Locate every blood parasite and identify its species.
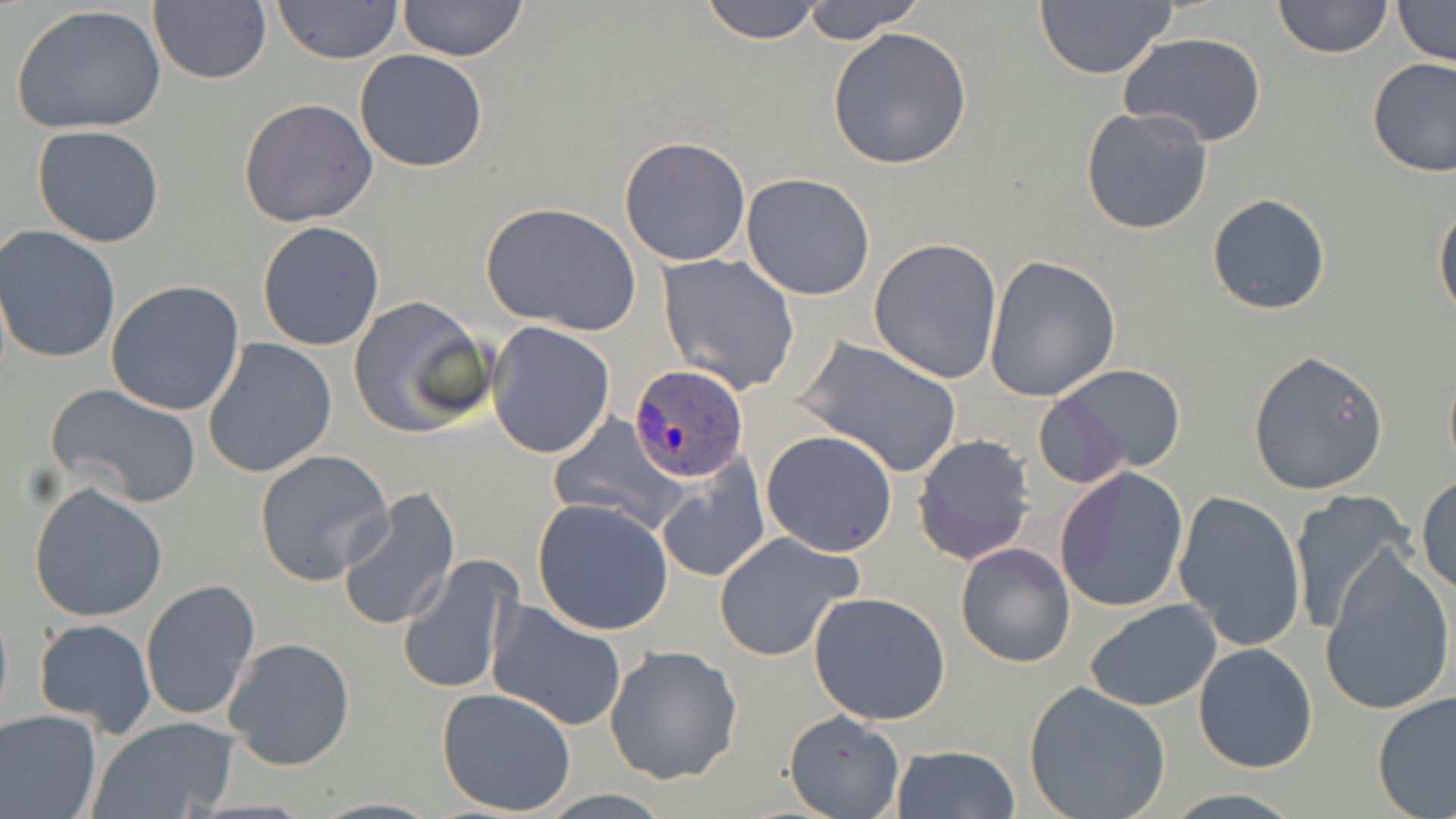

Approximate bounding boxes as [x1, y1, x2, y2] in pixels.
Plasmodium ovale-infected red blood cells: [628, 363, 749, 482].
No Plasmodium falciparum, Plasmodium malariae, Plasmodium vivax, Babesia divergens, or Trypanosoma brucei observed.

Uninfected red blood cell locations: [149, 0, 272, 85], [396, 0, 530, 63], [699, 0, 828, 43], [798, 0, 927, 43], [1273, 0, 1393, 58], [1391, 0, 1456, 67], [271, 1, 404, 65], [1034, 2, 1177, 79], [8, 3, 167, 137], [826, 27, 972, 168], [1119, 33, 1267, 148], [355, 48, 489, 172], [1365, 57, 1456, 177], [238, 98, 378, 228], [1081, 107, 1214, 235], [31, 124, 166, 247], [618, 135, 752, 267], [741, 173, 876, 301], [1206, 193, 1331, 315], [1433, 199, 1456, 326], [481, 201, 641, 336], [257, 221, 385, 351], [0, 226, 122, 365], [869, 237, 1002, 384], [657, 253, 800, 394], [983, 255, 1120, 402], [105, 280, 246, 416], [347, 296, 492, 439], [486, 323, 616, 458], [798, 335, 963, 478], [202, 338, 337, 478], [1246, 349, 1389, 496], [1442, 360, 1456, 482], [1042, 364, 1188, 479], [46, 382, 202, 509], [548, 414, 686, 534], [761, 430, 898, 557], [911, 433, 1035, 566], [253, 448, 394, 586], [655, 457, 771, 581], [1053, 465, 1190, 614], [1416, 475, 1455, 593], [28, 481, 169, 623], [334, 489, 460, 633], [1173, 489, 1307, 651], [1287, 492, 1416, 636], [532, 499, 674, 636], [712, 530, 865, 663], [954, 541, 1075, 669], [1320, 546, 1455, 718], [398, 555, 521, 696], [139, 580, 261, 725], [807, 590, 953, 726], [484, 600, 628, 731], [1084, 600, 1222, 712], [32, 618, 157, 738], [222, 636, 355, 771], [1193, 641, 1319, 774], [604, 644, 742, 785], [1023, 681, 1172, 819], [436, 687, 577, 817], [1372, 691, 1456, 819], [0, 707, 102, 819], [784, 709, 906, 818], [89, 718, 240, 818], [889, 743, 1021, 819]. Slide-level diagnosis: Plasmodium ovale. May-Grünwald-Giemsa stain. One field of a larger specimen. Image is 1456×819 pixels. 1000x magnification. Light microscopy. Thin blood film.